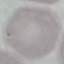
{
  "result": "no malaria parasites seen",
  "image_type": "automatically extracted cell patch, resized to 64 × 64 pixels",
  "preparation": "thin blood film",
  "stain": "Giemsa",
  "capture": "smartphone camera at the microscope eyepiece"
}